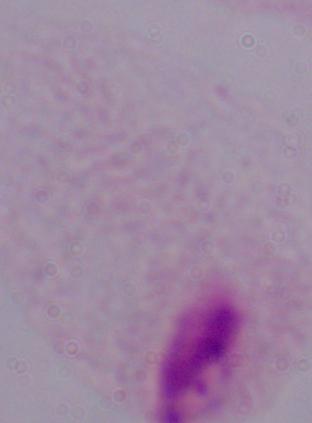
identification = trichomonad
modality = photomicrograph
magnification = 1000x